State which parasite is depicted.
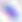
This is Toxoplasma gondii.

magnification = 400x
modality = photomicrograph